Assess this cell for malaria.
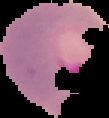

Parasitized.

From a thin blood film. Image is 109×118 pixels. Cell region segmented out of the field of view; the surrounding area is masked to black.